Identify the parasite.
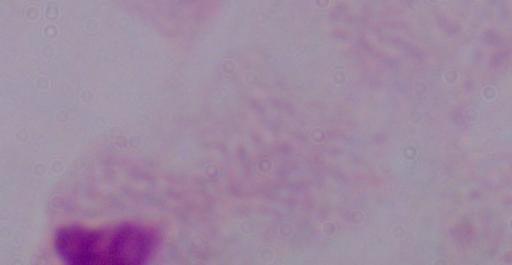
This is a trichomonad.

modality: photomicrograph
magnification: 1000x